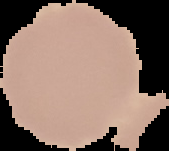
Summary:
  - Result: negative for malaria parasites
  - Image size: 169×151 pixels
  - Image type: segmented cell region on a black background
  - Preparation: thin blood smear